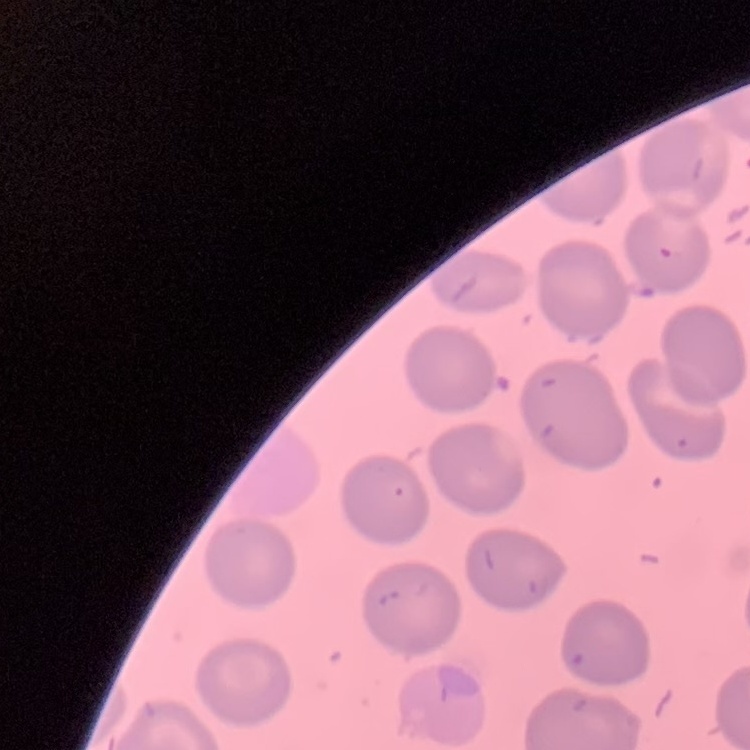
Summary:
  - Erythrocyte morphology: no rouleaux formation
  - Stain: Field's or Giemsa
  - Preparation: thin blood smear
  - Image type: one tile cut from a larger photomicrograph